Identify the blood parasite species.
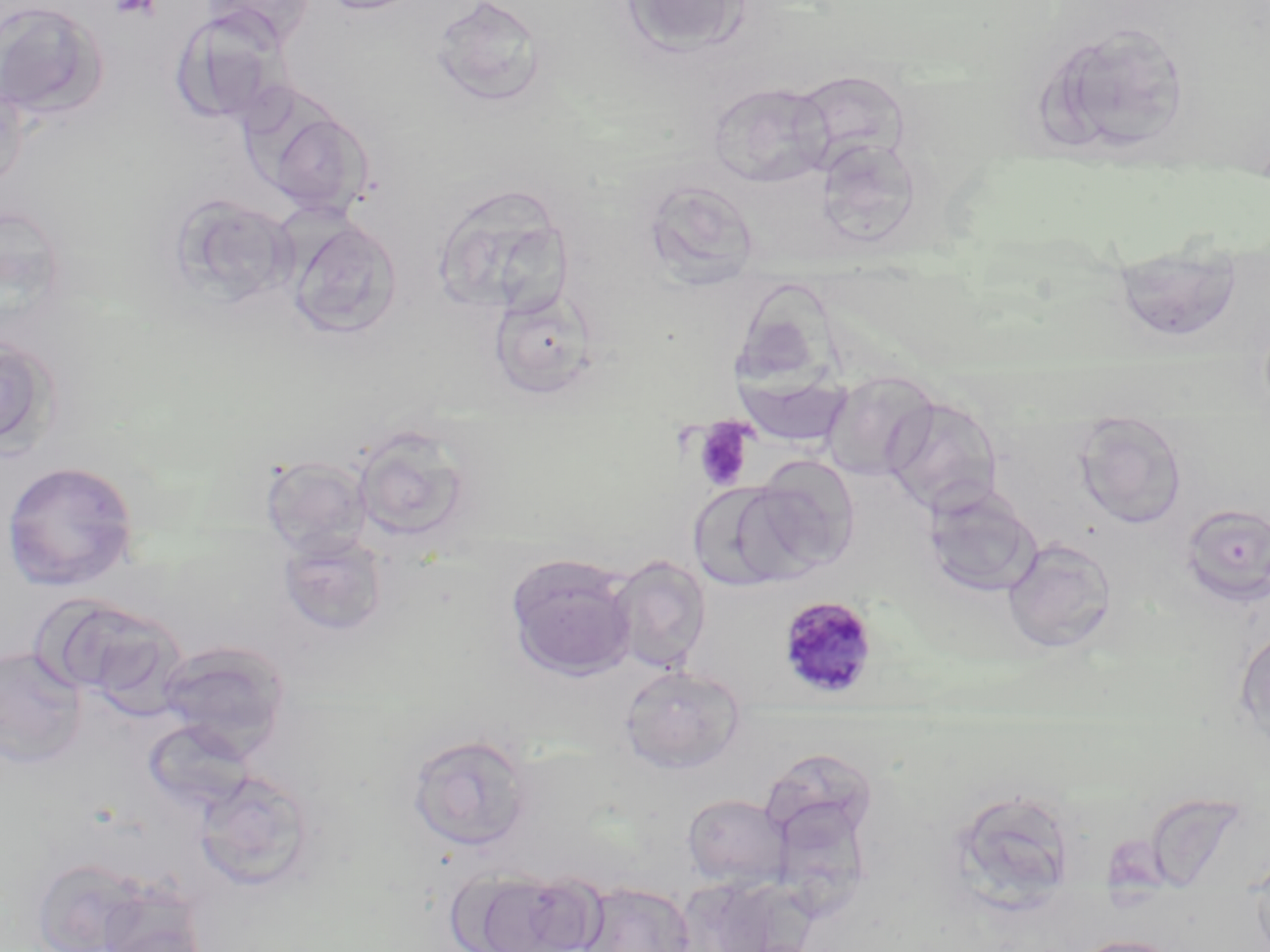
Plasmodium malariae.

Approximate bounding boxes as (x1,y1)-(x2,y2) corner pairs in pixels. Uninfected red blood cell locations: (318,0)-(428,15), (430,0)-(549,107), (619,0)-(752,56), (0,2)-(108,120), (170,9)-(289,128), (1036,18)-(1192,159), (790,69)-(911,175), (0,76)-(30,194), (708,82)-(833,188), (258,104)-(375,220), (815,136)-(923,248), (432,182)-(575,316), (649,183)-(764,296), (169,194)-(298,308), (287,218)-(403,339), (1110,240)-(1246,344), (488,287)-(599,400), (0,331)-(59,457), (822,370)-(939,482), (737,371)-(854,449), (881,395)-(1004,517), (1074,416)-(1188,528), (351,426)-(475,545), (261,455)-(372,559), (744,456)-(859,578), (1,460)-(140,591), (688,481)-(807,592), (922,483)-(1043,598), (1180,503)-(1270,607), (278,531)-(390,636), (1002,536)-(1118,654), (505,553)-(637,680), (607,555)-(711,673), (54,598)-(190,712), (1234,626)-(1270,750), (158,641)-(291,756), (0,647)-(87,766), (619,664)-(745,774), (142,718)-(256,814), (407,733)-(533,851), (194,769)-(315,891), (947,788)-(1079,914), (682,793)-(790,890), (768,797)-(875,925), (1249,851)-(1270,952), (31,857)-(153,952), (462,870)-(600,952), (676,875)-(789,952), (576,881)-(696,952), (88,882)-(211,952), (1067,934)-(1188,952). Platelet locations: (108,0)-(161,20), (693,419)-(753,491). Plasmodium malariae-infected red blood cell locations: (777,595)-(880,701). Single field of view. Thin blood film. Optical microscopy. Image is 1270×952 pixels. 1000x magnification. May-Grünwald-Giemsa-stained preparation.